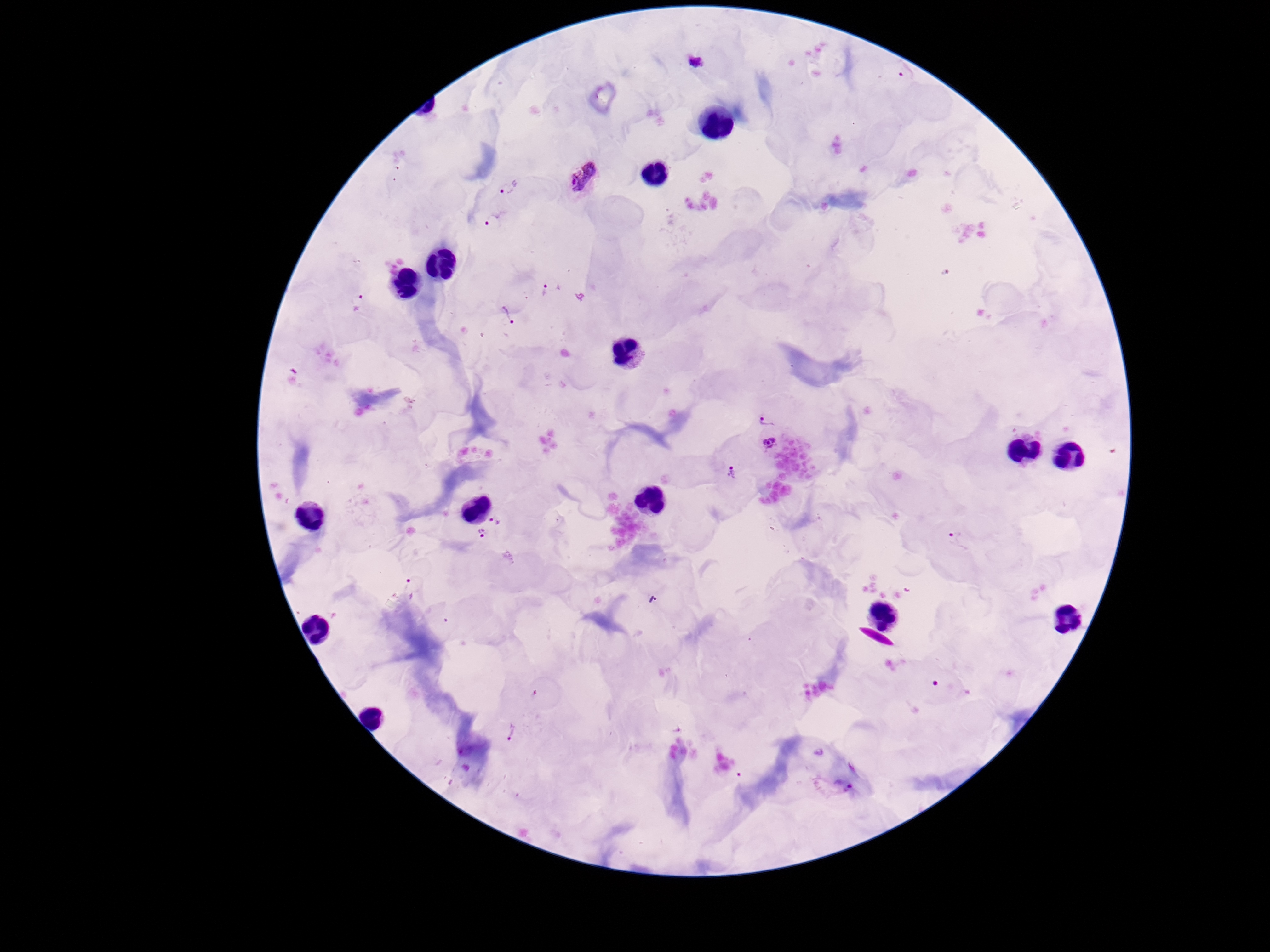 Approximate centers as [x, y] in pixels. Plasmodium parasite locations: [695, 65], [585, 179], [509, 187], [493, 219], [550, 288], [357, 304], [508, 315], [765, 419], [769, 443], [731, 473], [496, 520], [482, 533], [960, 540], [414, 588], [511, 734], [833, 787]. 100x magnification. Giemsa-stained preparation. Patient malaria status: infected. Image is 1270×952 pixels. Photographed through the microscope eyepiece with a smartphone camera. One field from this slide. Thick blood film.